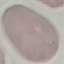

malaria status = uninfected
preparation = thin blood smear
capture = smartphone through the microscope eyepiece
stain = Giemsa
image type = cell patch, automatically extracted from a larger field of view and resized to 64 × 64 pixels